Assess the morphology of the erythrocytes.
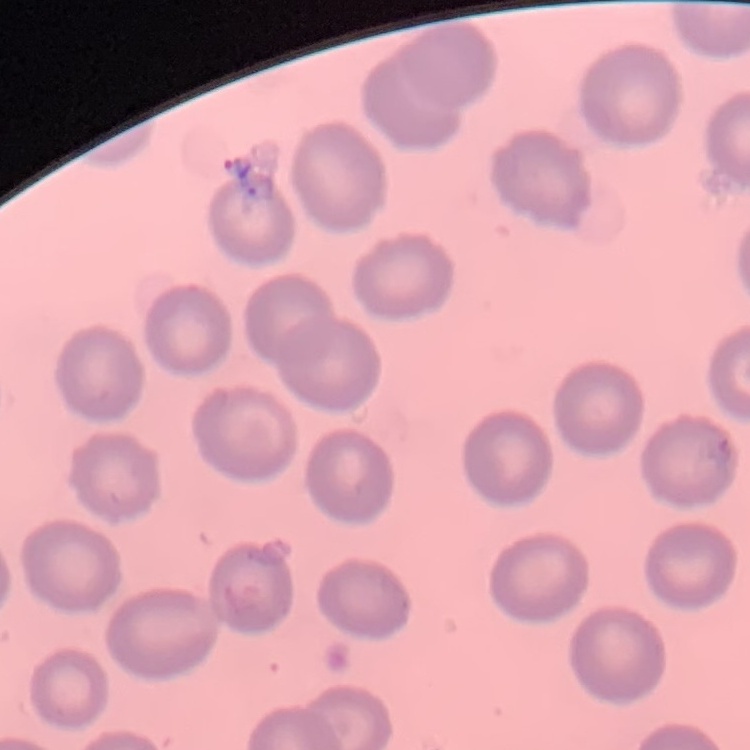

No rouleaux formation.

Summary:
  - Stain: Field's or Giemsa
  - Preparation: thin blood smear
  - Image type: one tile cut from a larger photomicrograph